State which cell type is depicted.
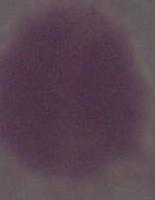
This is an erythrocyte.

Micrograph. Captured at 1000x magnification.